Locate and identify every blood parasite.
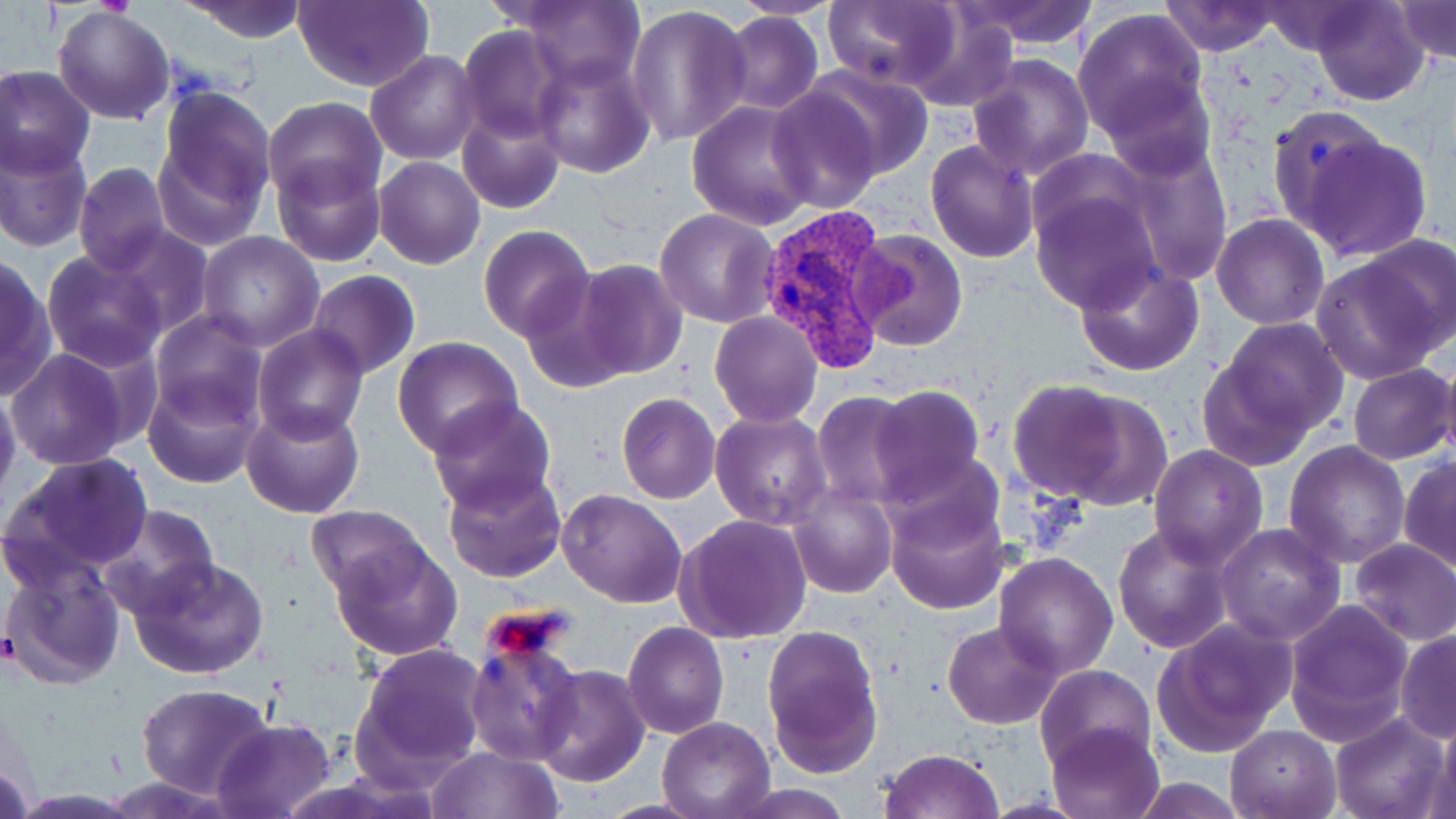

Approximate bounding boxes as (x1,y1)-(x2,y2) corner pairs in pixels.
Plasmodium vivax-infected red blood cells: (757,205)-(895,376).
No Plasmodium falciparum, Plasmodium ovale, Plasmodium malariae, Babesia divergens, or Trypanosoma brucei observed.

slide-level diagnosis = Plasmodium vivax
stain = May-Grünwald-Giemsa
image size = 1456×819 pixels
preparation = thin blood smear
field of view = single
magnification = 1000x
uninfected red blood cell locations = approximate bounding boxes as (x1,y1)-(x2,y2) corner pairs in pixels: (293,0)-(432,91), (729,0)-(841,19), (954,0)-(1099,49), (1156,0)-(1285,56), (1311,0)-(1429,107), (179,1)-(312,43), (1394,1)-(1455,66), (518,2)-(645,87), (823,2)-(959,90), (1256,3)-(1379,56), (626,4)-(752,148), (53,7)-(175,125), (1072,7)-(1208,138), (901,9)-(1019,113), (723,11)-(822,114), (457,25)-(566,143), (366,50)-(481,165), (533,51)-(654,178), (967,53)-(1095,180), (0,65)-(95,177), (806,66)-(935,184), (1101,77)-(1217,181), (766,84)-(884,213), (153,85)-(276,242), (262,96)-(385,205), (688,101)-(817,230), (458,106)-(565,213), (1266,107)-(1391,238), (1297,129)-(1434,260), (0,137)-(91,252), (926,138)-(1039,262), (1119,142)-(1233,284), (272,157)-(386,267), (375,157)-(486,269), (74,162)-(171,276), (1029,184)-(1162,313), (655,208)-(781,329), (1212,214)-(1329,329), (101,224)-(213,341), (478,225)-(595,343), (850,229)-(967,351), (196,231)-(324,352), (1360,234)-(1455,350), (42,249)-(169,371), (0,254)-(55,400), (1310,255)-(1444,385), (573,258)-(688,381), (1074,258)-(1203,375), (307,270)-(420,378), (522,275)-(632,396), (149,309)-(269,428), (709,311)-(823,427), (1211,318)-(1349,447), (253,325)-(369,444), (393,337)-(524,458), (6,348)-(131,470), (1436,349)-(1456,469), (1200,354)-(1317,472), (1347,363)-(1455,465), (144,372)-(261,489), (1005,378)-(1151,505), (0,384)-(21,500), (866,385)-(987,501), (617,393)-(721,504), (812,393)-(917,508), (425,396)-(556,516), (240,401)-(365,518), (711,411)-(830,529), (1284,441)-(1412,569), (1150,445)-(1267,568), (3,453)-(153,581), (1399,455)-(1456,574), (441,467)-(567,585), (789,484)-(896,598), (558,489)-(688,609), (886,490)-(1009,615), (96,504)-(219,621), (306,505)-(428,603), (675,515)-(812,645), (1112,522)-(1234,652), (1215,523)-(1346,646), (330,537)-(464,660), (1350,538)-(1456,645), (994,552)-(1119,676), (2,553)-(125,686), (125,556)-(270,679), (1284,598)-(1413,746), (945,620)-(1063,729), (1152,620)-(1295,755), (622,621)-(730,740), (761,624)-(883,775), (1394,630)-(1456,742), (353,644)-(489,782), (466,653)-(583,773), (1034,664)-(1156,774), (533,666)-(649,787), (136,682)-(274,799), (1330,712)-(1450,819), (657,716)-(776,819), (212,719)-(337,819), (1046,721)-(1165,818), (1428,721)-(1456,817), (1224,722)-(1342,818), (427,746)-(563,819), (881,748)-(1003,819), (1130,777)-(1249,817), (725,782)-(858,817)
modality = optical microscopy